Report the malaria status of this cell.
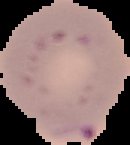
It is parasitized.

Summary:
  - Image size: 130×145 pixels
  - Image type: segmented cell region with the area outside set to black
  - Preparation: thin blood smear